Outline each uninfected red blood cell.
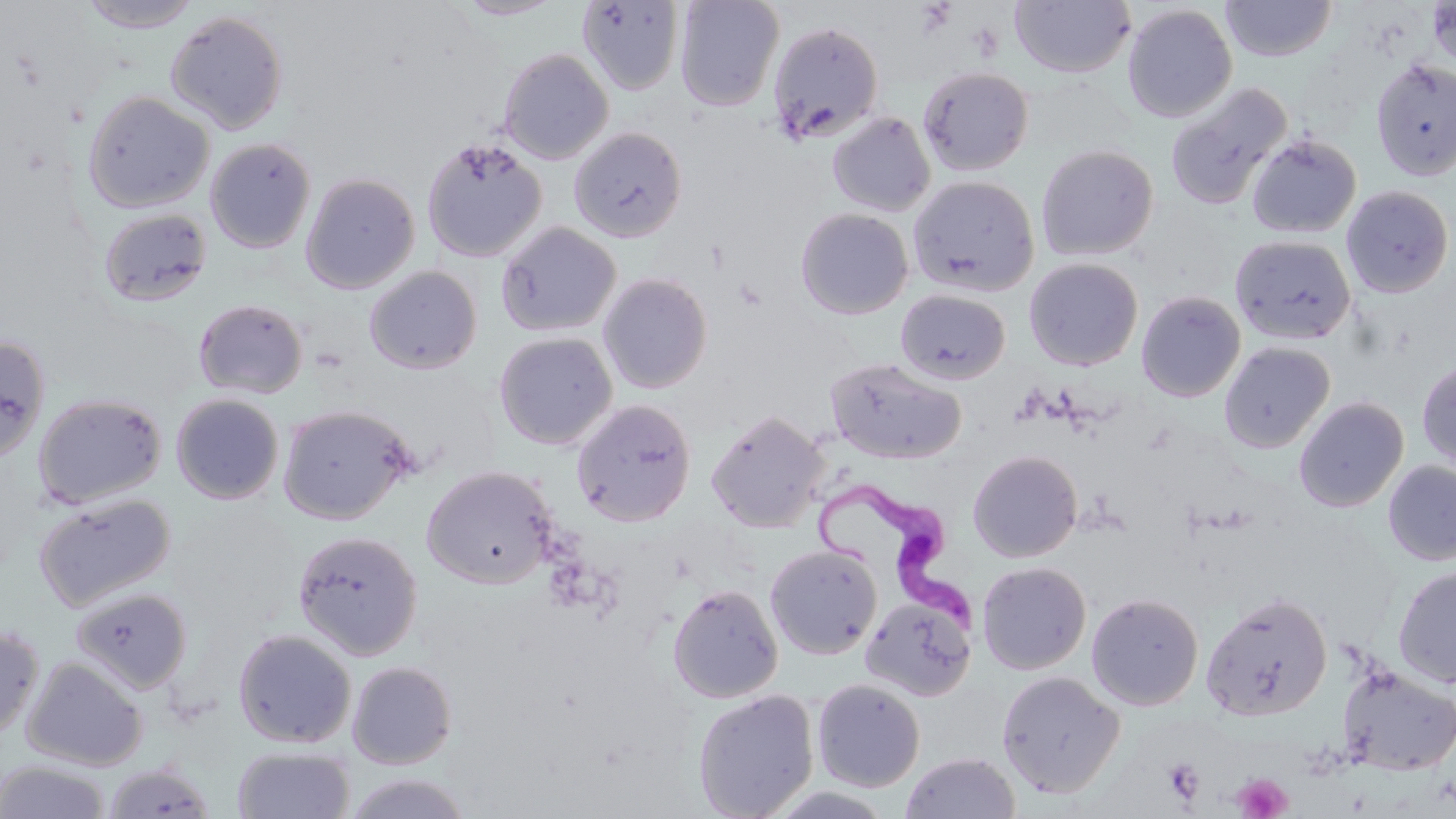
Approximate bounding boxes as named x1/y1/x2/y2 corners in pixels.
Uninfected red blood cells: (x1=453, y1=0, x2=564, y2=20), (x1=674, y1=0, x2=784, y2=112), (x1=1220, y1=0, x2=1337, y2=61), (x1=77, y1=1, x2=204, y2=32), (x1=577, y1=1, x2=685, y2=95), (x1=1010, y1=1, x2=1135, y2=79), (x1=1427, y1=1, x2=1456, y2=72), (x1=1122, y1=4, x2=1237, y2=122), (x1=165, y1=11, x2=288, y2=135), (x1=767, y1=21, x2=884, y2=145), (x1=498, y1=48, x2=613, y2=164), (x1=1370, y1=57, x2=1456, y2=181), (x1=917, y1=65, x2=1034, y2=177), (x1=1165, y1=82, x2=1293, y2=211), (x1=83, y1=90, x2=214, y2=213), (x1=827, y1=111, x2=936, y2=217), (x1=569, y1=127, x2=687, y2=242), (x1=1246, y1=133, x2=1361, y2=238), (x1=205, y1=137, x2=316, y2=254), (x1=421, y1=137, x2=547, y2=262), (x1=1036, y1=144, x2=1158, y2=261), (x1=301, y1=172, x2=420, y2=294), (x1=908, y1=175, x2=1039, y2=296), (x1=1341, y1=185, x2=1454, y2=298), (x1=98, y1=208, x2=212, y2=308), (x1=794, y1=208, x2=914, y2=320), (x1=496, y1=221, x2=621, y2=337), (x1=1231, y1=235, x2=1355, y2=345), (x1=1024, y1=258, x2=1143, y2=371), (x1=364, y1=266, x2=482, y2=375), (x1=597, y1=272, x2=713, y2=394), (x1=895, y1=288, x2=1011, y2=385), (x1=1136, y1=291, x2=1246, y2=402), (x1=193, y1=298, x2=308, y2=399), (x1=493, y1=331, x2=618, y2=450), (x1=0, y1=334, x2=50, y2=462), (x1=1219, y1=341, x2=1335, y2=453), (x1=825, y1=357, x2=966, y2=464), (x1=1417, y1=359, x2=1456, y2=472), (x1=33, y1=393, x2=167, y2=509), (x1=171, y1=393, x2=284, y2=504), (x1=1294, y1=396, x2=1409, y2=512), (x1=571, y1=399, x2=696, y2=526), (x1=277, y1=404, x2=416, y2=525), (x1=706, y1=408, x2=829, y2=532), (x1=968, y1=449, x2=1083, y2=562), (x1=1383, y1=460, x2=1456, y2=566), (x1=421, y1=465, x2=558, y2=589), (x1=34, y1=493, x2=174, y2=611), (x1=292, y1=531, x2=424, y2=661), (x1=765, y1=544, x2=883, y2=660), (x1=976, y1=562, x2=1091, y2=674), (x1=1393, y1=564, x2=1456, y2=688), (x1=667, y1=584, x2=783, y2=703), (x1=70, y1=586, x2=193, y2=694), (x1=1200, y1=591, x2=1333, y2=722), (x1=1086, y1=592, x2=1204, y2=710), (x1=860, y1=594, x2=976, y2=702), (x1=0, y1=626, x2=44, y2=741), (x1=232, y1=629, x2=357, y2=748), (x1=22, y1=657, x2=148, y2=771), (x1=346, y1=660, x2=457, y2=769), (x1=1337, y1=665, x2=1456, y2=776), (x1=996, y1=670, x2=1125, y2=797), (x1=812, y1=678, x2=925, y2=792), (x1=692, y1=689, x2=819, y2=819), (x1=232, y1=746, x2=354, y2=819), (x1=899, y1=751, x2=1022, y2=819), (x1=0, y1=760, x2=110, y2=819), (x1=102, y1=763, x2=215, y2=819), (x1=345, y1=772, x2=472, y2=819), (x1=761, y1=785, x2=900, y2=818).

slide-level diagnosis = Trypanosoma brucei
magnification = 1000x
Trypanosoma brucei locations = approximate bounding boxes as named x1/y1/x2/y2 corners in pixels: (x1=812, y1=475, x2=987, y2=643)
preparation = thin blood smear
platelet locations = approximate bounding boxes as named x1/y1/x2/y2 corners in pixels: (x1=1163, y1=758, x2=1205, y2=805), (x1=1233, y1=772, x2=1292, y2=818)
image size = 1456×819 pixels
field of view = one of a larger specimen
modality = optical microscopy
stain = May-Grünwald-Giemsa